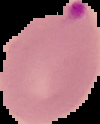
result = Plasmodium parasites identified
image type = segmented cell region with the area outside set to black
image size = 100×124 pixels
preparation = thin blood film